Assess the morphology of the red blood cells.
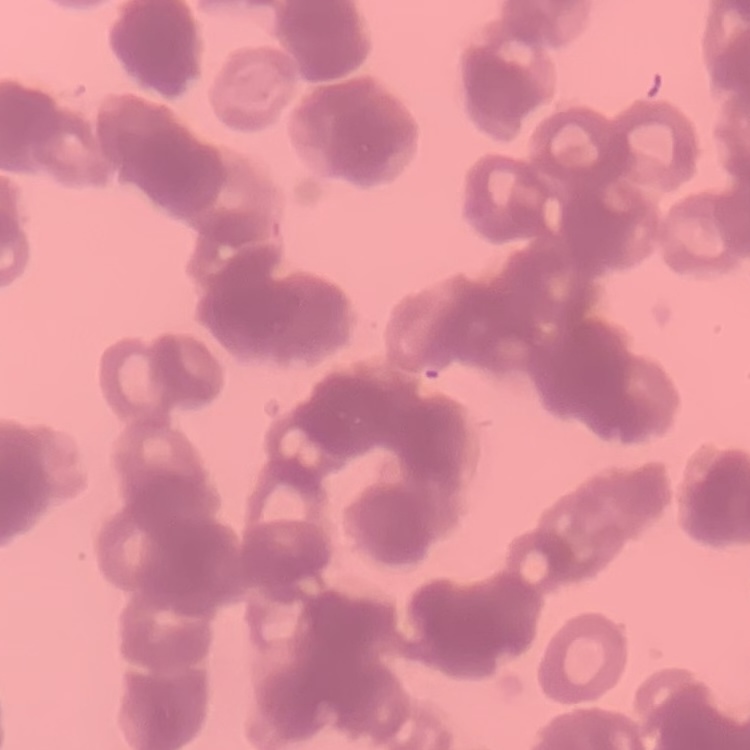

Rouleaux formation.

Thin blood film. One tile cut from a larger photomicrograph. Stained with either Field's or Giemsa.